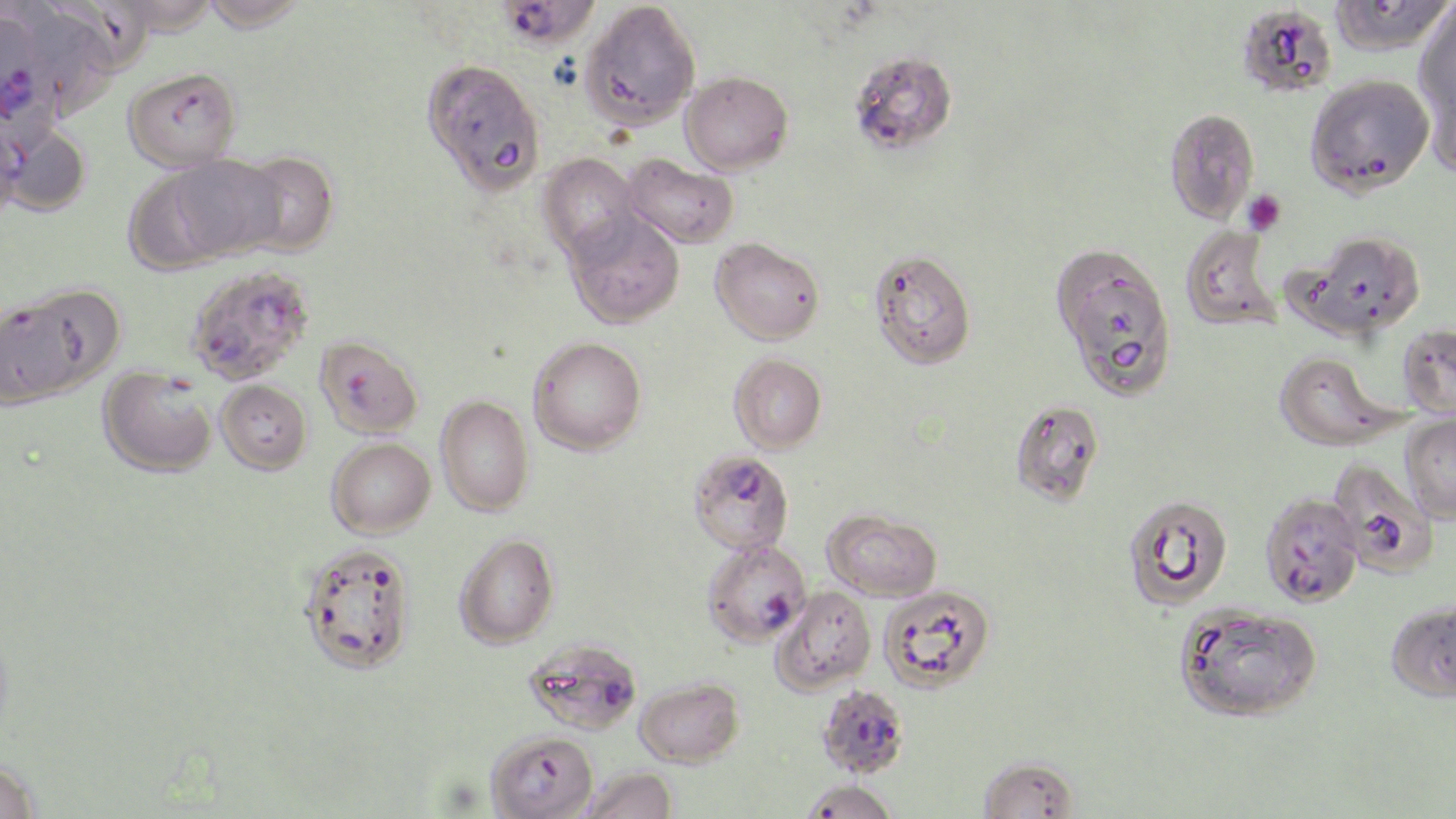 Approximate bounding boxes as (x1,y1)-(x2,y2) corner pairs in pixels. Uninfected red blood cell locations: (110,0)-(218,36), (198,0)-(311,33), (1328,0)-(1454,57), (580,1)-(701,130), (1415,3)-(1456,126), (26,6)-(119,122), (422,58)-(546,195), (123,66)-(242,171), (680,71)-(793,175), (1304,73)-(1434,198), (1163,108)-(1260,224), (0,114)-(27,223), (2,123)-(91,216), (231,150)-(339,256), (169,154)-(283,260), (538,154)-(642,263), (623,154)-(738,249), (122,169)-(231,276), (564,213)-(684,328), (1179,225)-(1283,333), (1291,229)-(1428,339), (711,237)-(825,344), (869,249)-(976,369), (1,287)-(114,406), (1397,323)-(1456,419), (528,336)-(646,454), (1273,351)-(1398,451), (729,353)-(827,453), (99,367)-(217,477), (216,379)-(312,474), (436,395)-(533,516), (1009,400)-(1104,507), (1401,413)-(1456,523), (327,438)-(435,538), (1122,493)-(1233,609), (823,508)-(942,601), (454,533)-(558,648), (296,542)-(416,674), (878,585)-(995,693), (773,586)-(876,693), (1385,599)-(1456,703), (1174,602)-(1324,723), (635,677)-(744,767), (485,730)-(598,818), (977,755)-(1078,818), (0,758)-(41,819), (581,766)-(678,819), (800,780)-(900,819). Plasmodium falciparum-infected red blood cell locations: (500,2)-(606,52), (1235,4)-(1337,98), (1,15)-(44,136), (850,51)-(958,155), (1050,244)-(1178,402), (185,264)-(314,385), (314,335)-(423,438), (689,450)-(794,555), (1329,459)-(1442,579), (1259,492)-(1364,608), (701,539)-(811,647), (525,637)-(642,734), (816,685)-(910,779). Platelet locations: (1242,189)-(1287,235). Slide-level diagnosis: Plasmodium falciparum. 1000x magnification. Light microscopy. One field of a larger specimen. Thin blood smear. May-Grünwald-Giemsa-stained preparation. Image is 1456×819 pixels.